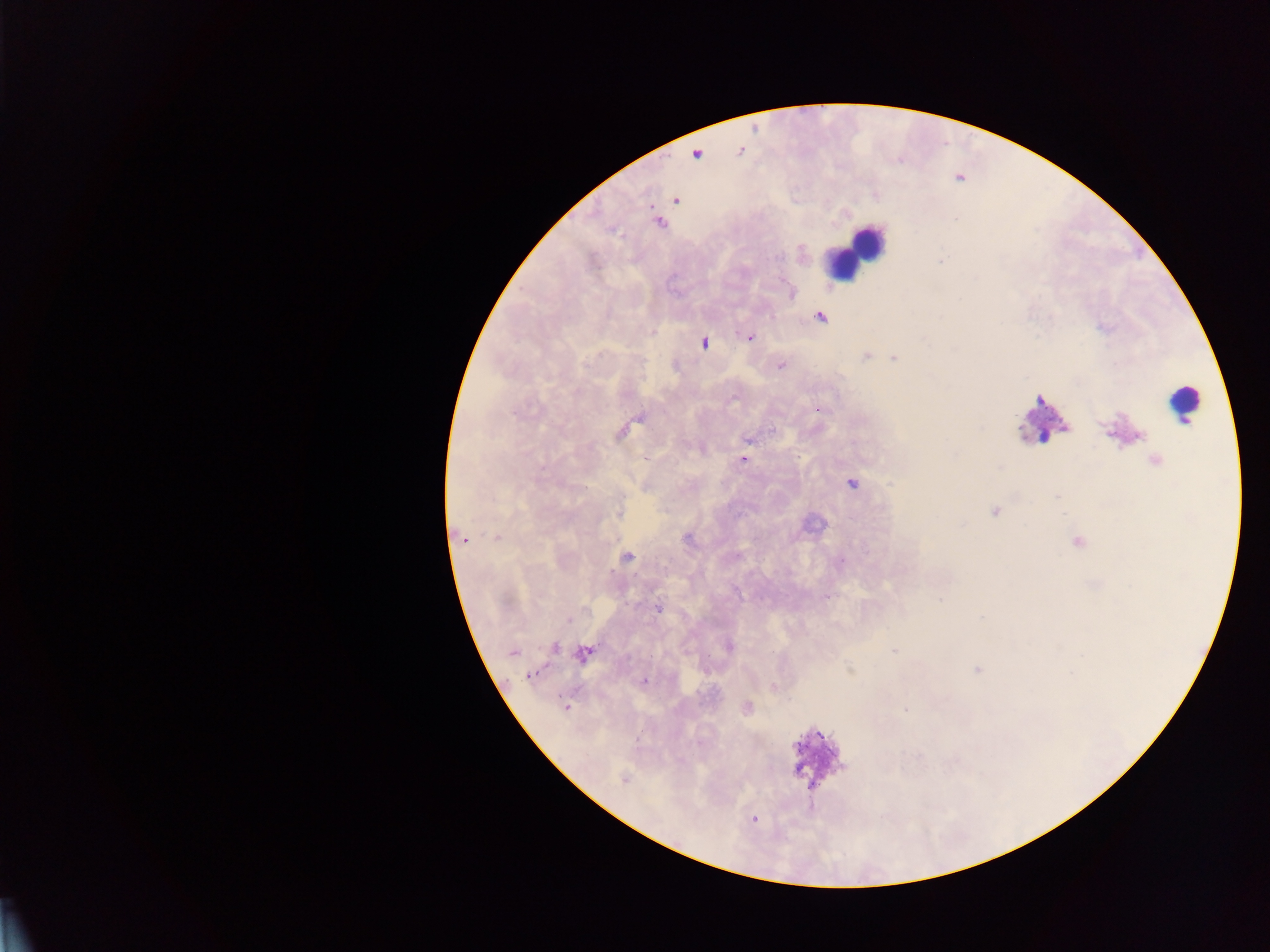
{
  "image_size": "1270×952 pixels",
  "malaria_parasite_locations": "approximate centers as [x, y] in pixels: [740, 151], [696, 153], [675, 200], [658, 223], [819, 317], [749, 337], [703, 343], [867, 355], [893, 358], [780, 365], [819, 408], [622, 429], [748, 438], [648, 457], [742, 459], [1156, 462], [851, 482], [996, 511], [619, 512], [496, 537], [461, 538], [1076, 542], [625, 556], [826, 596], [657, 607], [553, 646], [728, 646], [894, 651], [512, 652], [583, 653], [978, 669], [530, 674], [643, 680], [774, 686], [565, 707], [746, 707], [907, 709], [624, 779], [753, 819]",
  "capture": "mobile-phone photograph through a microscope",
  "preparation": "thick blood smear",
  "field_of_view": "single",
  "country": "Ghana",
  "leukocyte_locations": "approximate centers as [x, y] in pixels: [855, 252], [1184, 404], [1042, 419], [816, 758]"
}